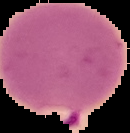
{
  "image_size": "130×133 pixels",
  "result": "malaria parasites detected",
  "preparation": "thin blood film",
  "image_type": "cell region segmented out of the field of view; surrounding area masked to black"
}